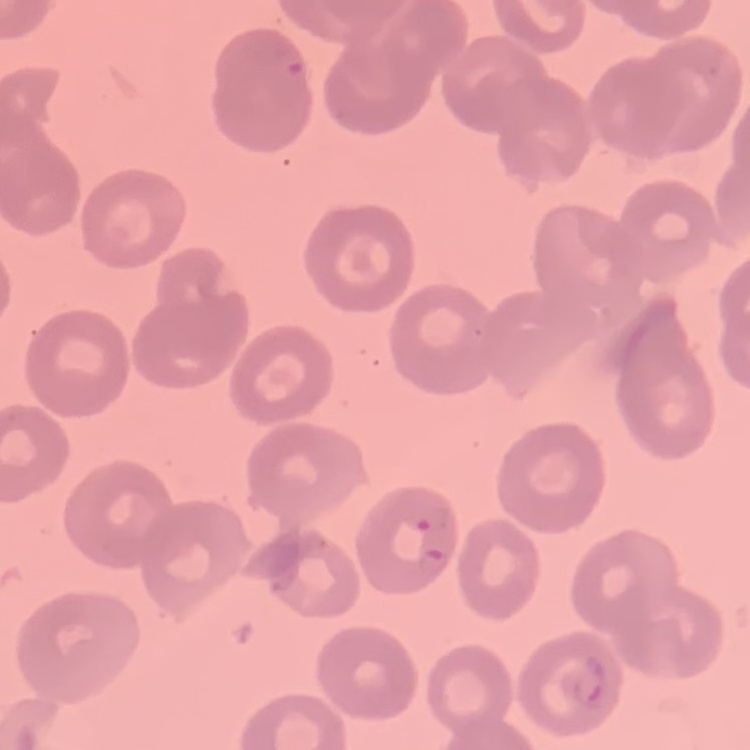

Summary:
  - Red blood cell morphology: no rouleaux formation
  - Stain: Field's or Giemsa
  - Preparation: thin blood film
  - Image type: one tile cut from a larger photomicrograph